Assess the morphology of the red blood cells.
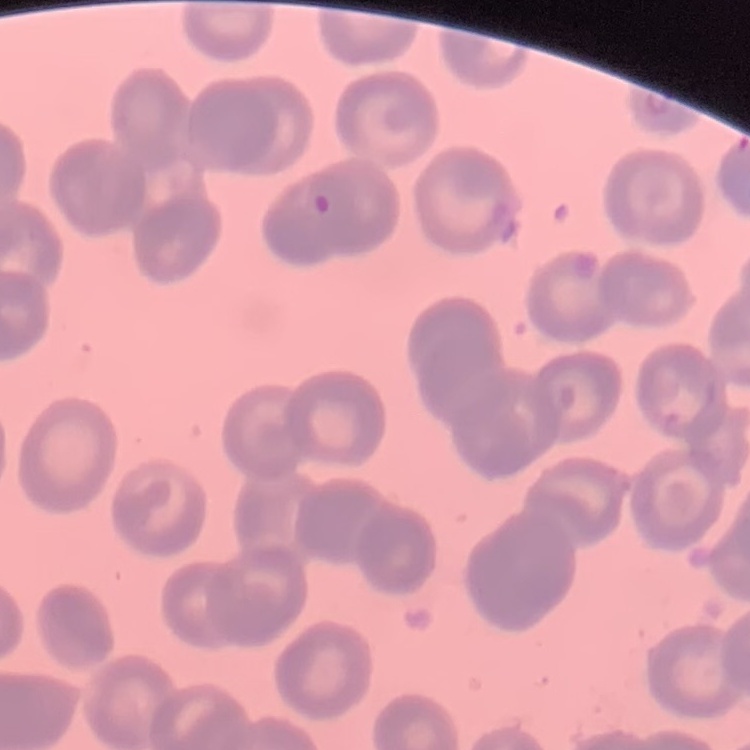

No rouleaux formation.

Thin peripheral smear. One tile cut from a larger photomicrograph. Stained with either Field's or Giemsa.